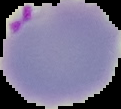 Image is 121×109 pixels. Cell region segmented out of the field of view; the surrounding area is masked to black. From a thin blood film. Malaria status: parasitized.